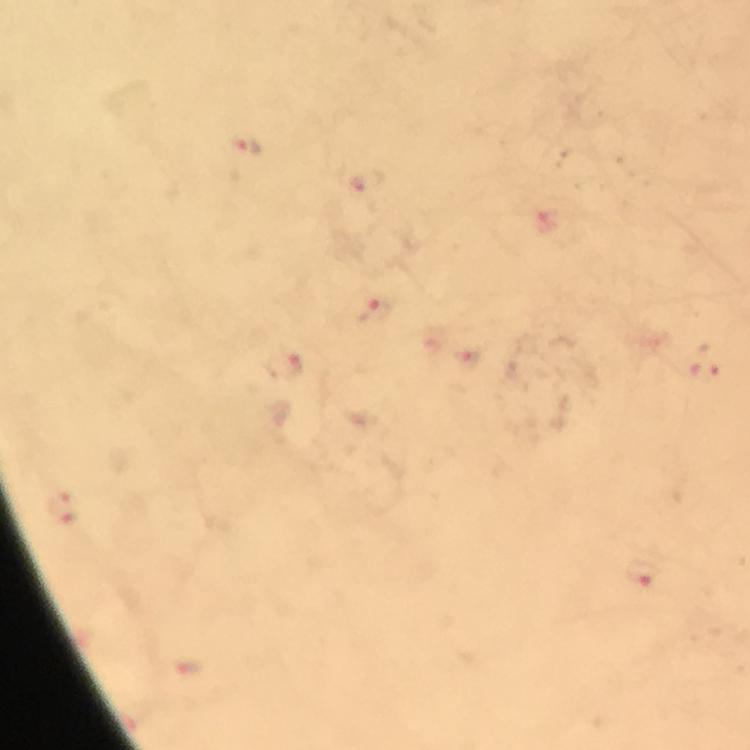

Approximate centers as [x, y] in pixels.
Summary:
  - Malaria parasite locations: [247, 146], [362, 181], [544, 220], [377, 311], [282, 363], [706, 372], [62, 510], [642, 571]
  - Capture: smartphone camera through the microscope
  - Preparation: thick blood smear
  - Stain: Giemsa
  - Cropped from: one field of view
  - Immersion oil: applied
  - Image size: 750×750 pixels
  - Context: from a malaria diagnostic workup
  - Magnification: 100x